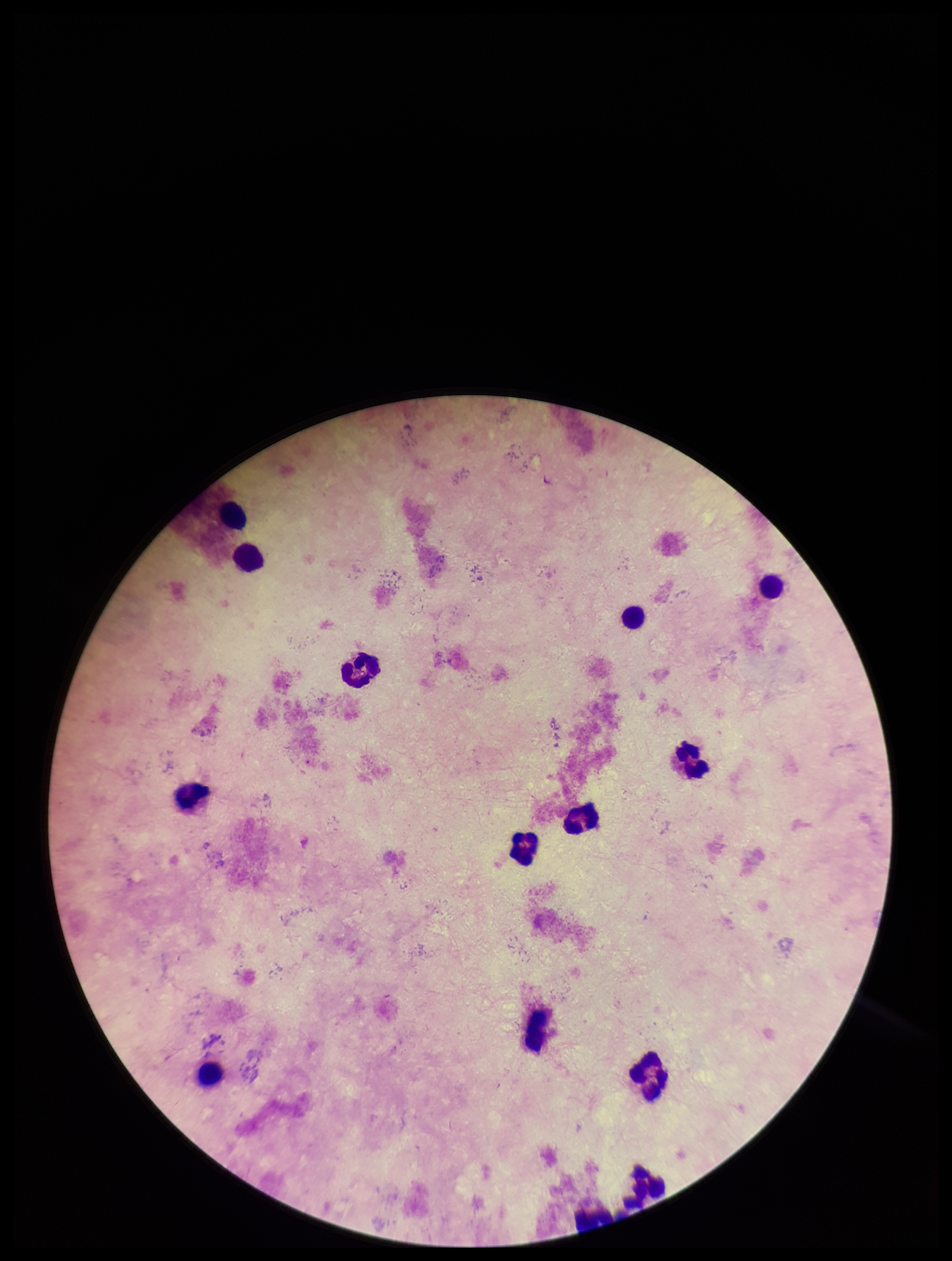

Summary:
  - Leukocyte count: 14
  - Image size: 952×1261 pixels
  - Parasite count: 0
  - Stain: Giemsa
  - Capture: smartphone photograph through the microscope eyepiece
  - Preparation: thick smear
  - Field of view: single
  - Plasmodium parasites: none seen
  - Patient malaria status: negative